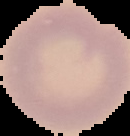 The area outside the segmented cell region is set to black. Image is 130×136 pixels. Malaria status: uninfected. From a thin blood smear.